Name the parasite shown.
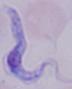
A trypanosome.

{
  "modality": "micrograph",
  "magnification": "1000x"
}